Name the cell type shown.
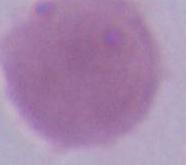
This is an erythrocyte.

modality = photomicrograph
magnification = 1000x